Comment on the morphology of the red blood cells.
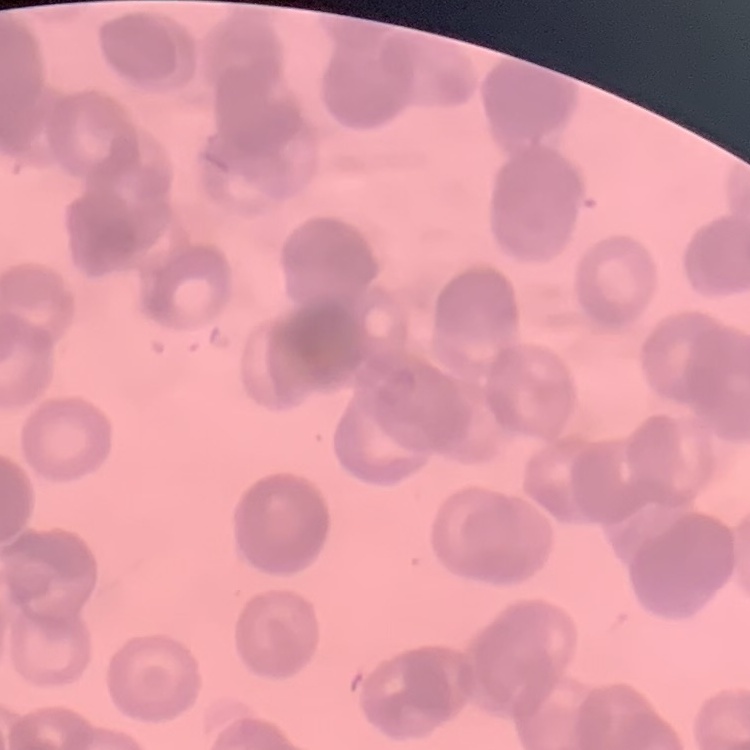
Rouleaux formation.

Summary:
  - Image type: square crop of a larger photomicrograph
  - Stain: Field's or Giemsa
  - Preparation: thin blood smear